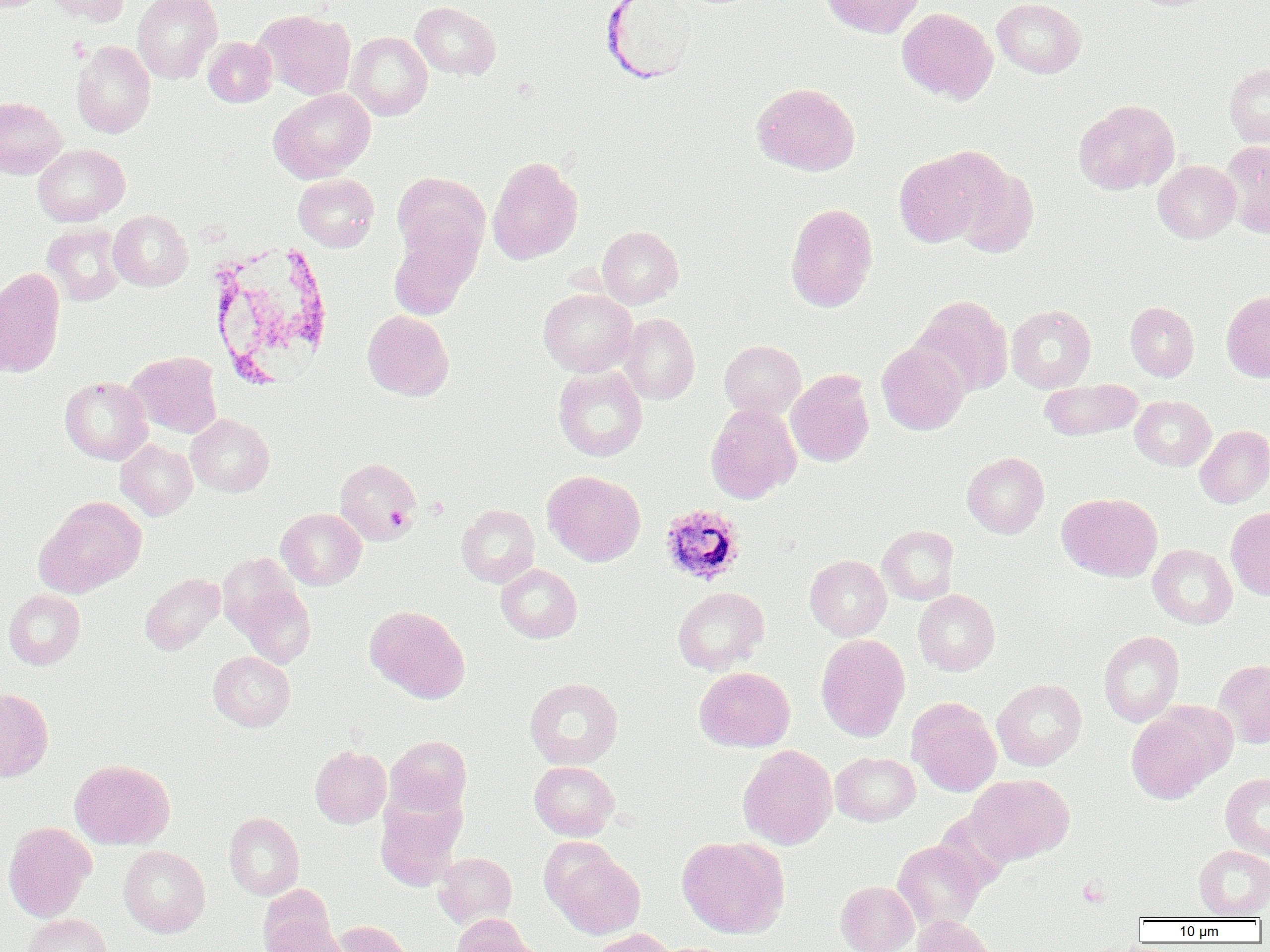

Summary:
  - Coordinate format: approximate bounding boxes as named x1/y1/x2/y2 corners in pixels
  - Plasmodium ovale-infected red blood cell locations: (x1=659, y1=505, x2=745, y2=585)
  - Platelet locations: (x1=388, y1=506, x2=411, y2=532), (x1=1078, y1=879, x2=1109, y2=906)
  - Uninfected red blood cell locations: (x1=44, y1=0, x2=130, y2=25), (x1=132, y1=0, x2=222, y2=83), (x1=821, y1=0, x2=925, y2=38), (x1=992, y1=0, x2=1086, y2=78), (x1=410, y1=1, x2=501, y2=80), (x1=897, y1=8, x2=997, y2=103), (x1=255, y1=9, x2=356, y2=100), (x1=345, y1=32, x2=432, y2=120), (x1=203, y1=37, x2=276, y2=107), (x1=72, y1=41, x2=155, y2=138), (x1=1225, y1=63, x2=1270, y2=148), (x1=751, y1=82, x2=860, y2=175), (x1=268, y1=88, x2=376, y2=182), (x1=0, y1=96, x2=67, y2=179), (x1=1073, y1=99, x2=1179, y2=194), (x1=1220, y1=141, x2=1270, y2=237), (x1=33, y1=144, x2=129, y2=226), (x1=894, y1=149, x2=996, y2=247), (x1=487, y1=156, x2=583, y2=264), (x1=1153, y1=160, x2=1240, y2=242), (x1=950, y1=162, x2=1039, y2=258), (x1=393, y1=171, x2=489, y2=267), (x1=293, y1=173, x2=379, y2=251), (x1=785, y1=203, x2=878, y2=312), (x1=109, y1=210, x2=192, y2=290), (x1=43, y1=223, x2=126, y2=305), (x1=387, y1=226, x2=479, y2=321), (x1=597, y1=226, x2=683, y2=308), (x1=0, y1=267, x2=66, y2=376), (x1=538, y1=288, x2=637, y2=376), (x1=1221, y1=291, x2=1270, y2=382), (x1=911, y1=295, x2=1014, y2=396), (x1=1125, y1=301, x2=1199, y2=381), (x1=1006, y1=304, x2=1096, y2=393), (x1=362, y1=310, x2=454, y2=400), (x1=619, y1=313, x2=700, y2=404), (x1=719, y1=340, x2=806, y2=419), (x1=876, y1=342, x2=969, y2=435), (x1=126, y1=351, x2=222, y2=437), (x1=553, y1=366, x2=647, y2=461), (x1=786, y1=369, x2=875, y2=467), (x1=60, y1=376, x2=153, y2=464), (x1=1039, y1=378, x2=1143, y2=441), (x1=1130, y1=395, x2=1215, y2=470), (x1=705, y1=403, x2=802, y2=503), (x1=186, y1=413, x2=274, y2=495), (x1=1195, y1=425, x2=1270, y2=507), (x1=116, y1=439, x2=198, y2=519), (x1=962, y1=452, x2=1049, y2=538), (x1=335, y1=457, x2=422, y2=545), (x1=543, y1=470, x2=645, y2=566), (x1=1057, y1=492, x2=1162, y2=581), (x1=35, y1=497, x2=146, y2=597), (x1=456, y1=504, x2=539, y2=587), (x1=1226, y1=507, x2=1270, y2=600), (x1=276, y1=508, x2=366, y2=589), (x1=878, y1=525, x2=958, y2=604), (x1=1148, y1=544, x2=1237, y2=628), (x1=805, y1=554, x2=892, y2=640), (x1=496, y1=563, x2=581, y2=643), (x1=140, y1=572, x2=225, y2=653), (x1=233, y1=581, x2=316, y2=668), (x1=673, y1=586, x2=769, y2=674), (x1=4, y1=589, x2=85, y2=669), (x1=913, y1=589, x2=1000, y2=675), (x1=365, y1=605, x2=470, y2=703), (x1=1099, y1=630, x2=1184, y2=726), (x1=816, y1=634, x2=910, y2=741), (x1=208, y1=650, x2=295, y2=731), (x1=1214, y1=660, x2=1270, y2=749), (x1=694, y1=666, x2=795, y2=752), (x1=525, y1=677, x2=623, y2=769), (x1=992, y1=678, x2=1087, y2=770), (x1=0, y1=688, x2=53, y2=781), (x1=907, y1=697, x2=1001, y2=796), (x1=1125, y1=704, x2=1232, y2=803), (x1=385, y1=736, x2=472, y2=817), (x1=737, y1=745, x2=837, y2=849), (x1=310, y1=746, x2=391, y2=827), (x1=830, y1=752, x2=919, y2=825), (x1=70, y1=759, x2=175, y2=849), (x1=529, y1=761, x2=618, y2=840), (x1=1220, y1=773, x2=1270, y2=860), (x1=966, y1=774, x2=1073, y2=864), (x1=375, y1=797, x2=464, y2=891), (x1=224, y1=812, x2=304, y2=900), (x1=3, y1=822, x2=96, y2=921), (x1=677, y1=836, x2=790, y2=939), (x1=892, y1=840, x2=986, y2=930), (x1=120, y1=845, x2=209, y2=937), (x1=1194, y1=845, x2=1270, y2=919), (x1=547, y1=847, x2=645, y2=939), (x1=433, y1=852, x2=517, y2=929), (x1=836, y1=881, x2=918, y2=952), (x1=258, y1=884, x2=336, y2=950), (x1=22, y1=914, x2=113, y2=952), (x1=913, y1=914, x2=996, y2=952), (x1=451, y1=915, x2=534, y2=952), (x1=264, y1=920, x2=352, y2=952), (x1=333, y1=920, x2=414, y2=952), (x1=591, y1=928, x2=678, y2=952)
  - White blood cell locations: (x1=205, y1=239, x2=334, y2=388)
  - Slide-level diagnosis: Plasmodium ovale
  - Preparation: thin blood film
  - Magnification: 1000x
  - Modality: light microscopy
  - Image size: 1270×952 pixels
  - Field of view: single